Name the parasite shown.
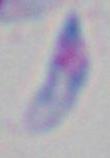
This is Toxoplasma gondii.

Micrograph. 1000x magnification.